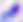
Micrograph. Toxoplasma gondii is shown. Captured at 400x magnification.